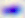 Toxoplasma gondii is seen. Captured at 400x magnification. Photomicrograph.